Name the cell type shown.
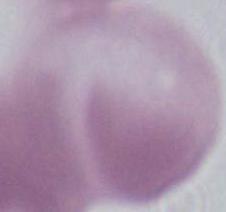

This is an erythrocyte.

Summary:
  - Magnification: 1000x
  - Modality: photomicrograph